Identify the parasite.
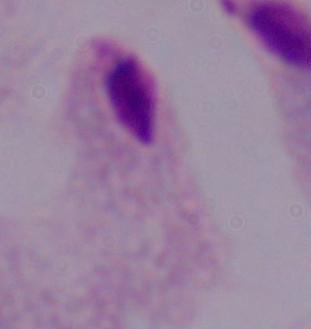
A trichomonad.

Summary:
  - Modality: photomicrograph
  - Magnification: 1000x